Point out malaria parasites and leukocytes.
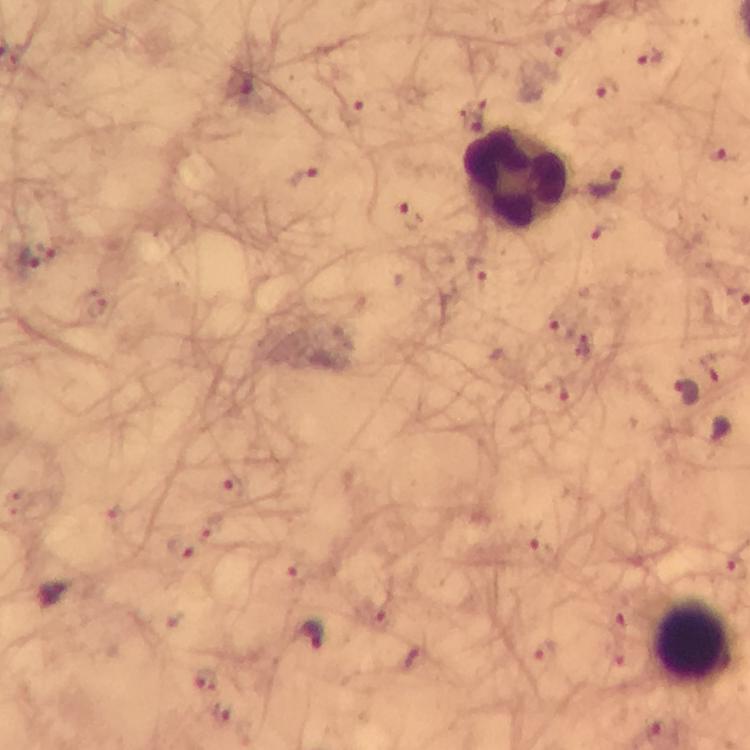

Approximate object centers, in pixels from the top-left corner.
Malaria parasites: (x=558, y=44), (x=649, y=53), (x=606, y=88), (x=607, y=182), (x=28, y=257), (x=562, y=326), (x=684, y=392), (x=540, y=541), (x=310, y=635), (x=544, y=652), (x=204, y=678).
Leukocytes: (x=518, y=179), (x=694, y=641).

Summary:
  - Preparation: thick blood film
  - Image size: 750×750 pixels
  - Immersion oil: applied
  - Context: from a diagnostic examination for malaria
  - Stain: Giemsa
  - Magnification: 100x
  - Capture: smartphone mounted on the microscope
  - Cropped from: one field of view